Assess the morphology of the red blood cells.
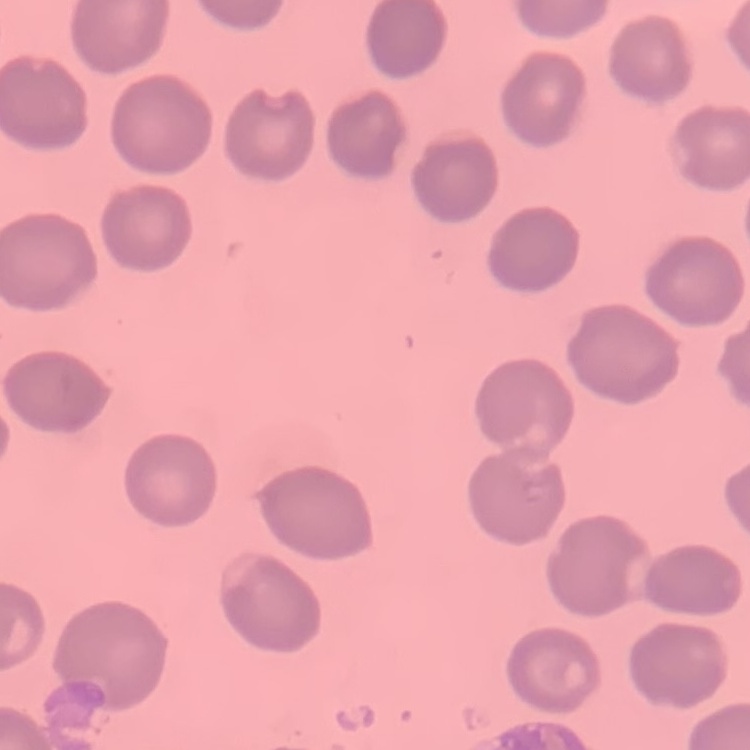

They show no rouleaux formation.

{
  "image_type": "square crop of a larger photomicrograph",
  "stain": "Field's or Giemsa",
  "preparation": "thin blood smear"
}